Classify this cell by malaria status.
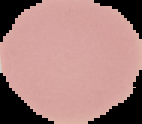

It is uninfected.

Summary:
  - Preparation: thin blood film
  - Image type: segmented cell region on a black background
  - Image size: 142×124 pixels